Identify the blood parasite species.
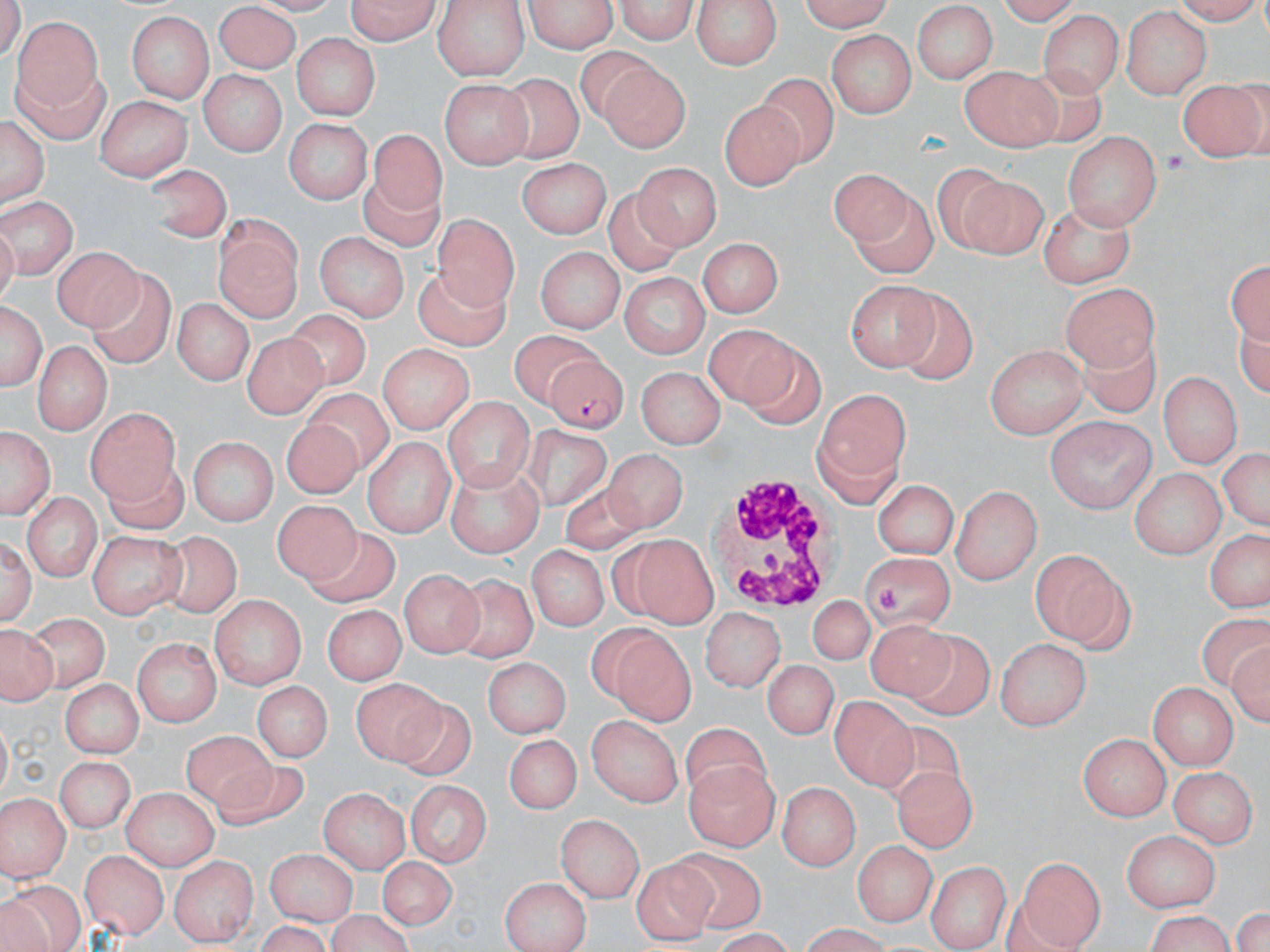
Plasmodium falciparum.

Summary:
  - Coordinate format: approximate bounding boxes as (x1, y1, x2, y2) in pixels
  - Plasmodium falciparum-infected red blood cell locations: (542, 356, 629, 434)
  - Platelet locations: (1164, 149, 1186, 174), (878, 586, 904, 613)
  - White blood cell locations: (708, 475, 844, 609)
  - Uninfected red blood cell locations: (338, 0, 443, 45), (521, 0, 622, 53), (612, 0, 700, 41), (691, 0, 784, 70), (796, 0, 894, 30), (993, 0, 1083, 27), (431, 1, 530, 78), (215, 3, 302, 74), (912, 3, 1001, 82), (1120, 6, 1210, 97), (1039, 10, 1122, 97), (126, 12, 212, 103), (12, 17, 101, 112), (111, 29, 200, 175), (829, 31, 912, 118), (293, 32, 381, 118), (576, 46, 659, 126), (599, 59, 690, 152), (962, 63, 1059, 152), (743, 65, 833, 173), (1019, 65, 1104, 146), (5, 66, 108, 142), (500, 68, 584, 162), (196, 70, 289, 156), (1179, 79, 1267, 159), (441, 80, 532, 167), (98, 95, 192, 182), (721, 96, 804, 192), (2, 113, 48, 207), (287, 119, 372, 203), (361, 128, 446, 235), (1063, 131, 1159, 229), (519, 158, 610, 238), (639, 162, 719, 252), (140, 163, 230, 241), (930, 165, 1012, 252), (829, 169, 928, 256), (958, 170, 1047, 257), (606, 184, 689, 273), (857, 190, 937, 276), (0, 197, 77, 275), (1040, 202, 1135, 289), (433, 212, 519, 302), (213, 214, 304, 319), (316, 235, 409, 322), (698, 237, 784, 322), (56, 245, 139, 333), (534, 245, 621, 333), (1229, 255, 1270, 346), (89, 267, 177, 371), (413, 268, 512, 352), (622, 271, 712, 359), (846, 281, 941, 371), (1063, 282, 1158, 371), (890, 290, 975, 385), (1, 296, 46, 395), (168, 297, 255, 385), (284, 309, 370, 387), (703, 323, 801, 405), (1071, 325, 1156, 410), (507, 329, 611, 396), (244, 333, 330, 416), (32, 338, 109, 433), (739, 341, 823, 432), (379, 343, 471, 434), (987, 343, 1085, 436), (642, 366, 723, 444), (1158, 371, 1240, 468), (814, 386, 911, 502), (300, 388, 394, 470), (443, 398, 534, 491), (87, 405, 177, 499), (1047, 415, 1154, 509), (284, 420, 364, 499), (0, 422, 55, 523), (520, 425, 608, 517), (363, 434, 452, 535), (187, 437, 276, 525), (1218, 444, 1267, 533), (606, 447, 685, 535), (99, 459, 191, 534), (442, 466, 543, 555), (1126, 469, 1226, 556), (874, 476, 958, 558), (558, 479, 639, 554), (952, 485, 1040, 583), (23, 492, 98, 582), (267, 500, 365, 588), (1205, 525, 1266, 617), (1, 527, 36, 628), (306, 530, 408, 605), (89, 531, 184, 619), (155, 533, 243, 621), (615, 533, 719, 626), (529, 541, 608, 629), (1029, 547, 1133, 650), (857, 554, 956, 631), (400, 568, 480, 658), (446, 573, 542, 661), (809, 594, 874, 666), (208, 596, 308, 692), (326, 606, 402, 681), (703, 607, 785, 694), (1196, 612, 1268, 692), (26, 613, 109, 686), (868, 619, 960, 707), (1, 620, 54, 707), (599, 623, 696, 723), (906, 631, 993, 720), (1227, 632, 1270, 728), (993, 634, 1089, 729), (135, 636, 222, 727), (485, 655, 571, 738), (762, 659, 840, 740), (349, 676, 448, 764), (56, 677, 146, 758), (251, 679, 333, 766), (1150, 681, 1237, 769), (832, 698, 915, 788), (394, 701, 474, 778), (585, 714, 686, 806), (872, 722, 967, 807), (678, 726, 772, 812), (1080, 731, 1172, 821), (504, 733, 579, 814), (181, 735, 279, 811), (55, 752, 137, 834), (684, 759, 779, 850), (892, 764, 975, 852), (211, 765, 308, 830), (1171, 765, 1254, 848), (781, 777, 861, 871), (407, 778, 493, 868), (320, 785, 411, 871), (120, 787, 216, 869), (0, 795, 68, 881), (559, 813, 645, 900), (1121, 828, 1218, 910), (853, 839, 934, 930), (265, 849, 360, 924), (660, 849, 766, 930), (80, 851, 167, 937), (170, 854, 257, 944), (374, 856, 459, 929), (1016, 856, 1103, 950), (632, 857, 714, 946), (928, 860, 1009, 951), (501, 875, 591, 952), (5, 886, 84, 951), (330, 906, 410, 951), (1141, 909, 1242, 952)
  - Image size: 1270×952 pixels
  - Field of view: single
  - Modality: optical microscopy
  - Stain: May-Grünwald-Giemsa
  - Preparation: thin blood film
  - Magnification: 1000x